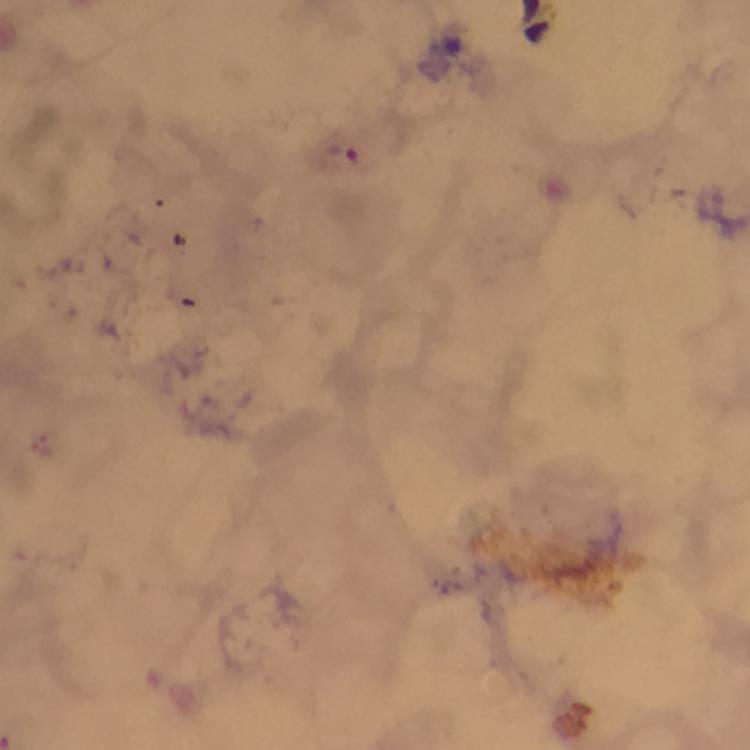
context = from a diagnostic examination for malaria
capture = smartphone photograph through a microscope
immersion oil = applied
stain = Giemsa
image size = 750×750 pixels
cropped from = a single field of view
preparation = thick blood smear
magnification = 100x
malaria parasite locations = approximate centers as {x, y} in pixels: {344, 152}